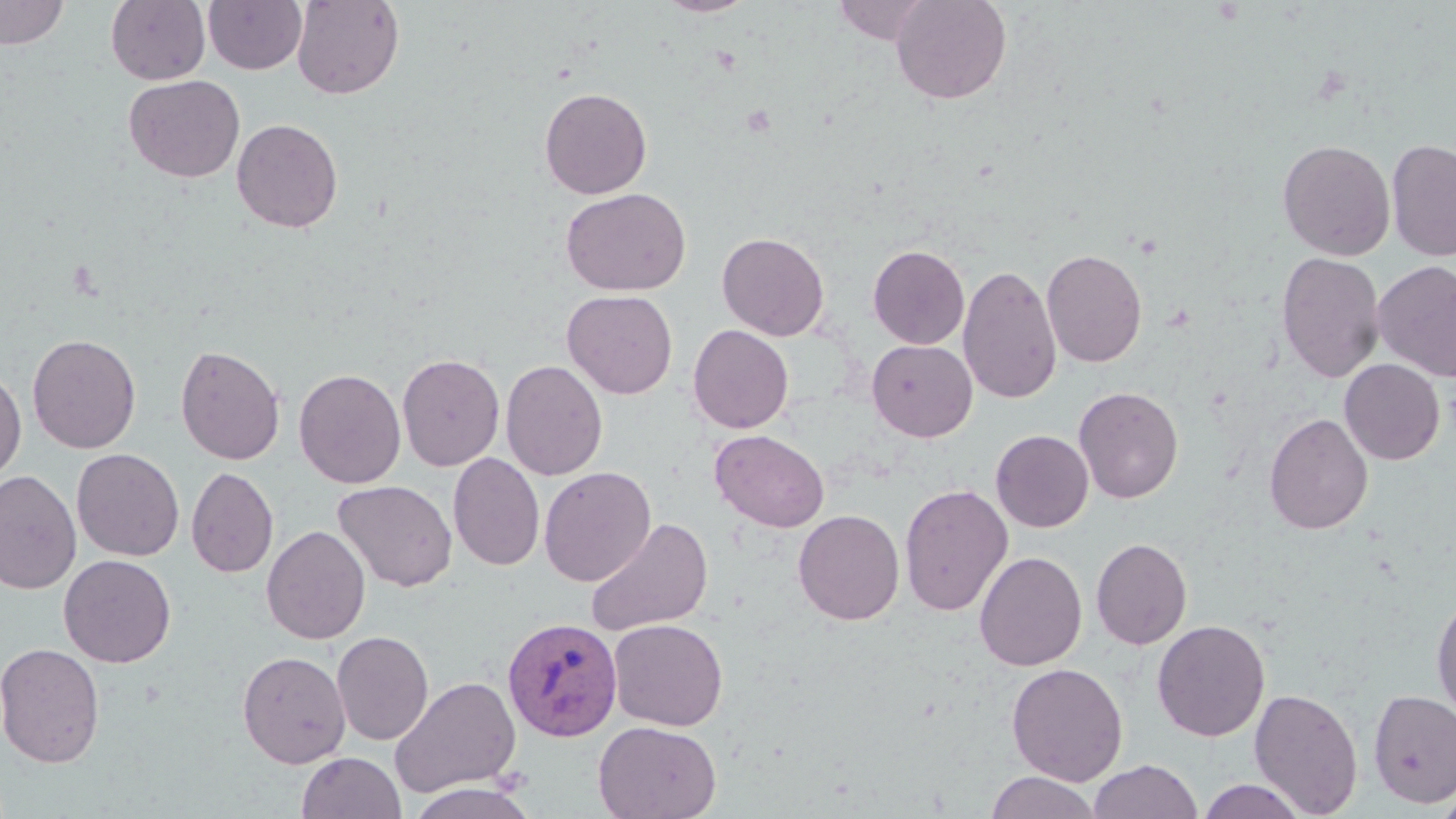

Approximate bounding boxes as (x1,y1)-(x2,y2) corner pairs in pixels. Plasmodium vivax-infected red blood cell locations: (502,617)-(622,741). Uninfected red blood cell locations: (0,0)-(69,49), (106,0)-(210,85), (203,0)-(307,74), (291,0)-(405,99), (656,0)-(758,17), (831,0)-(938,45), (890,0)-(1012,105), (123,74)-(245,183), (539,86)-(652,199), (232,118)-(343,233), (1386,138)-(1456,263), (1277,139)-(1396,260), (561,187)-(691,296), (717,232)-(829,341), (868,245)-(970,349), (1041,248)-(1148,367), (1276,251)-(1386,383), (1372,260)-(1456,382), (958,264)-(1062,404), (562,289)-(678,399), (688,324)-(794,433), (27,333)-(141,453), (867,340)-(977,442), (176,344)-(286,465), (397,353)-(505,471), (1339,359)-(1445,465), (500,360)-(608,481), (0,367)-(26,486), (294,368)-(406,489), (1073,385)-(1184,504), (1264,413)-(1373,535), (710,430)-(829,532), (991,430)-(1094,532), (71,448)-(184,561), (448,452)-(545,571), (539,466)-(656,587), (186,467)-(279,578), (0,469)-(82,595), (333,480)-(457,592), (899,484)-(1013,617), (793,509)-(905,625), (585,516)-(713,638), (261,525)-(371,645), (1091,537)-(1192,650), (974,551)-(1087,671), (59,554)-(176,667), (1431,592)-(1456,725), (608,618)-(728,731), (1152,619)-(1270,741), (332,630)-(434,745), (0,641)-(105,768), (237,650)-(352,769), (1006,662)-(1128,786), (390,675)-(521,799), (1249,688)-(1364,817), (1368,689)-(1456,808), (593,720)-(722,819), (296,752)-(406,819), (1087,759)-(1202,819), (984,772)-(1103,819), (1196,779)-(1309,819), (405,781)-(540,819), (1434,784)-(1456,819). Slide-level diagnosis: Plasmodium vivax. Light microscopy. Thin blood film. Captured at 1000x magnification. May-Grünwald-Giemsa-stained preparation. One field of a larger specimen. Image is 1456×819 pixels.